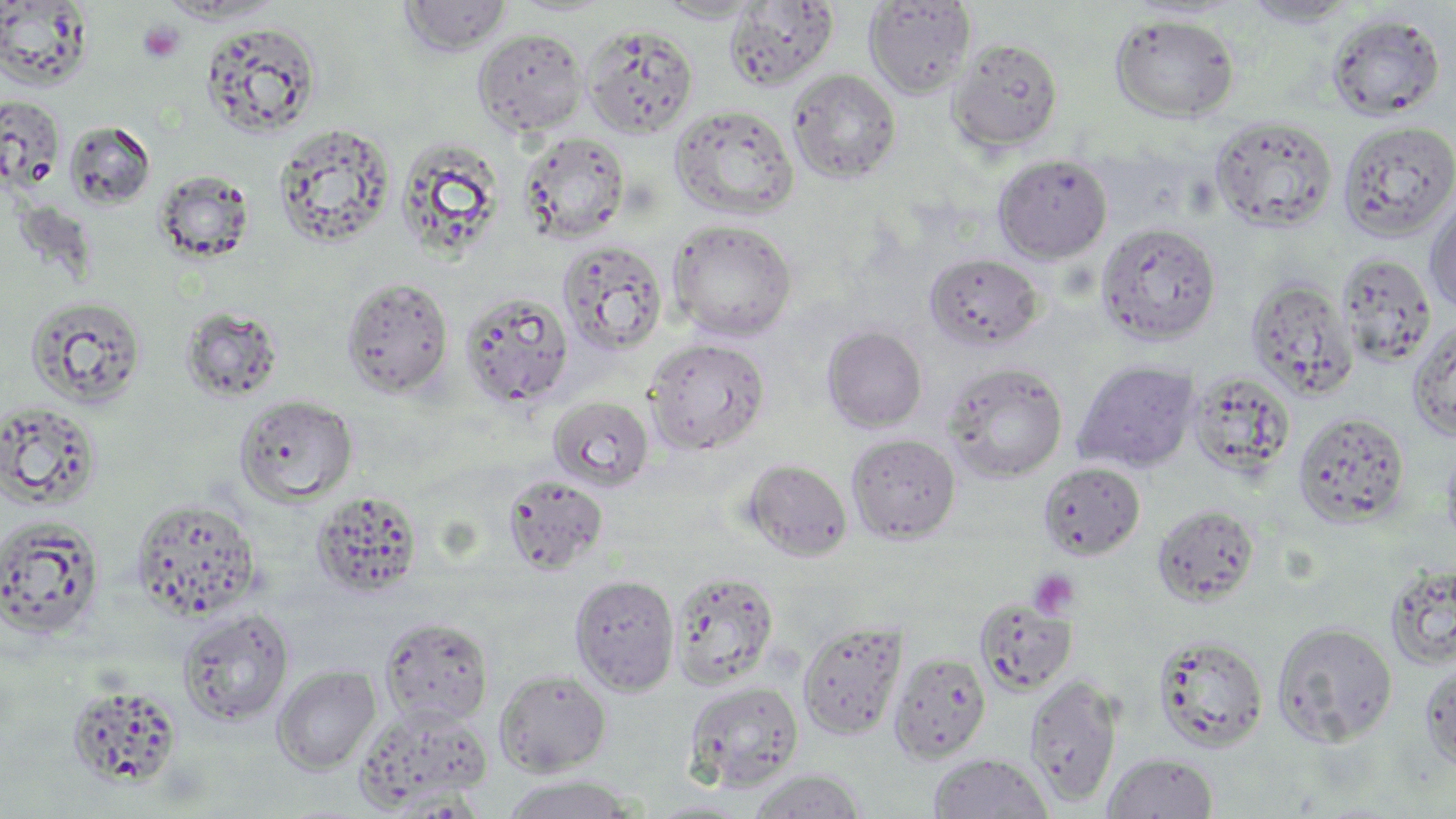 Approximate bounding boxes as (x1, y1, x2, y2) in pixels. Platelet locations: (138, 21, 184, 63), (1029, 569, 1080, 619). Uninfected red blood cell locations: (398, 0, 513, 56), (0, 1, 94, 91), (656, 1, 763, 22), (724, 1, 839, 91), (862, 1, 977, 99), (1243, 1, 1358, 27), (1326, 13, 1445, 121), (1110, 14, 1239, 123), (200, 20, 322, 139), (582, 23, 699, 138), (472, 27, 590, 136), (947, 37, 1063, 153), (787, 68, 901, 184), (0, 97, 65, 191), (669, 104, 799, 219), (1210, 115, 1338, 233), (1337, 119, 1456, 242), (64, 120, 156, 209), (272, 122, 396, 249), (518, 131, 631, 244), (395, 135, 506, 259), (993, 154, 1112, 263), (154, 169, 256, 264), (1424, 189, 1456, 316), (667, 219, 798, 341), (1095, 222, 1222, 345), (557, 239, 668, 358), (924, 253, 1044, 352), (1336, 253, 1436, 368), (340, 275, 454, 399), (1245, 277, 1356, 399), (458, 290, 575, 410), (24, 294, 147, 410), (179, 307, 284, 402), (1406, 322, 1456, 442), (822, 326, 927, 433), (643, 337, 771, 456), (1072, 360, 1200, 473), (942, 361, 1068, 483), (1188, 370, 1295, 477), (233, 394, 358, 507), (547, 395, 654, 492), (1, 402, 103, 510), (1292, 412, 1409, 529), (846, 433, 961, 544), (1441, 439, 1456, 553), (742, 449, 964, 554), (743, 459, 853, 562), (1038, 462, 1145, 560), (502, 474, 609, 576), (311, 490, 424, 598), (129, 496, 263, 621), (1152, 504, 1260, 606), (0, 516, 105, 641), (1385, 564, 1456, 671), (669, 569, 779, 690), (569, 574, 679, 695), (974, 598, 1077, 695), (177, 609, 295, 726), (379, 617, 494, 728), (797, 620, 907, 739), (1272, 620, 1398, 748), (1151, 634, 1269, 753), (888, 651, 992, 764), (1420, 660, 1456, 772), (271, 665, 381, 774), (494, 669, 611, 777), (1024, 675, 1124, 808), (683, 681, 805, 792), (65, 683, 184, 788), (355, 703, 491, 812), (927, 753, 1054, 818), (1102, 753, 1218, 818), (747, 770, 866, 818), (499, 775, 637, 818), (644, 797, 756, 817). Slide-level diagnosis: no evidence of blood parasites. 1000x magnification. Thin blood film. Image is 1456×819 pixels. Optical microscopy. One field of a larger specimen. May-Grünwald-Giemsa stain.